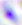

{
  "magnification": "400x",
  "identification": "Toxoplasma gondii",
  "modality": "micrograph"
}